Identify the cell.
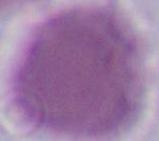

An erythrocyte.

modality = photomicrograph
magnification = 1000x